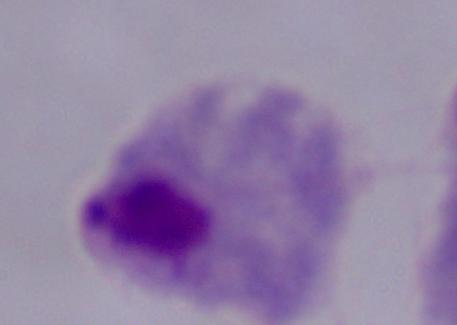
Summary:
  - Magnification: 1000x
  - Modality: micrograph
  - Identification: trichomonad